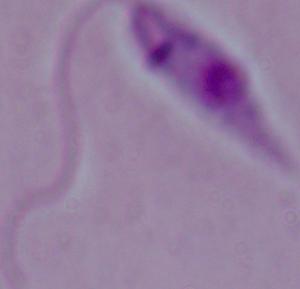

Summary:
  - Modality: micrograph
  - Identification: Leishmania
  - Magnification: 1000x